Classify this cell by malaria status.
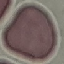
Uninfected.

Automatically extracted cell patch, resized to 64 × 64 pixels. Giemsa-stained preparation. Thin smear of blood. Photographed with a smartphone camera at the microscope eyepiece.